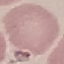

result = no malaria parasites seen
preparation = thin blood film
stain = Giemsa
capture = smartphone camera at the microscope eyepiece
image type = automatically extracted cell patch, resized to 64 × 64 pixels